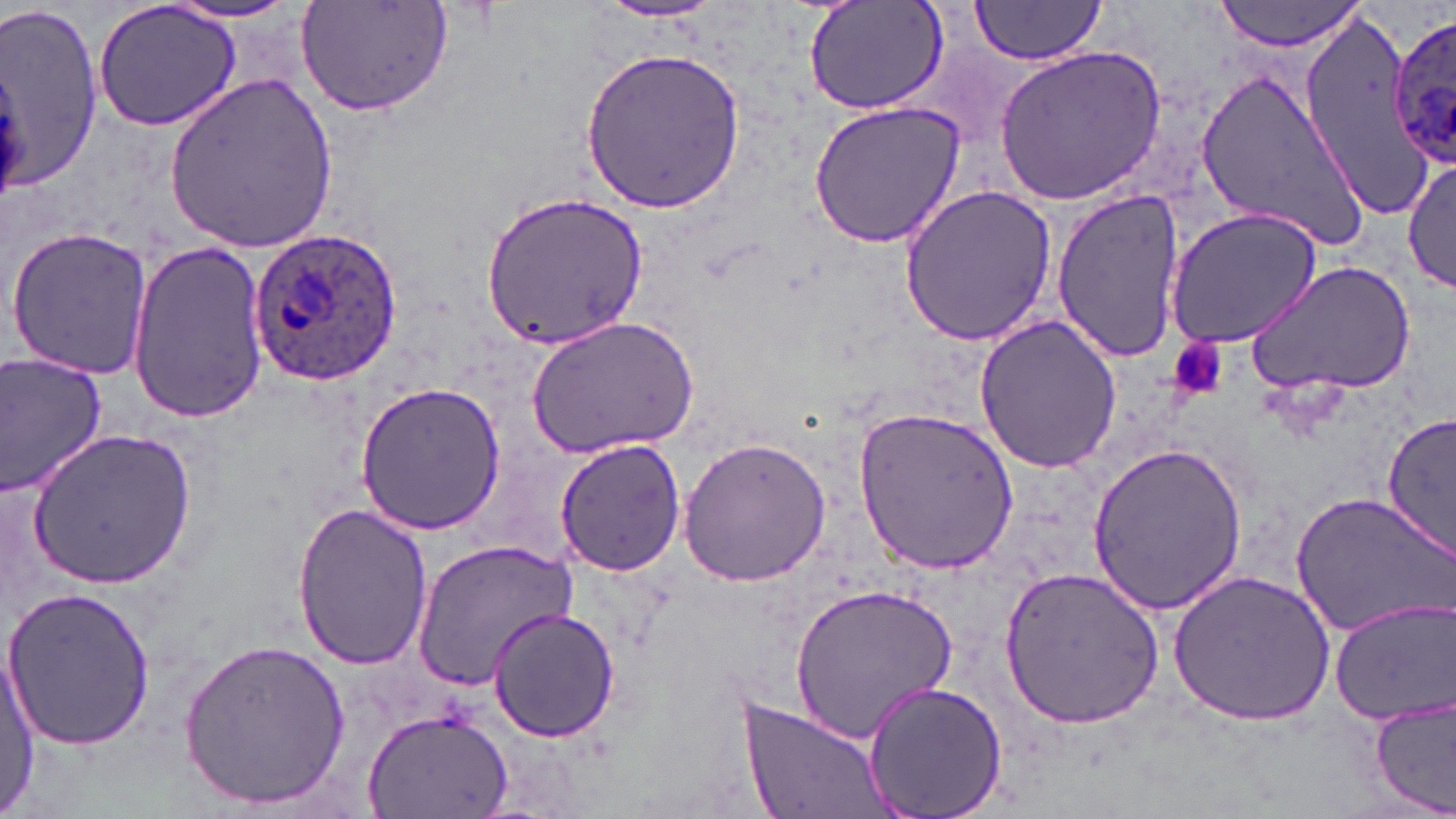

slide-level diagnosis = Plasmodium ovale
magnification = 1000x
preparation = thin blood smear
field of view = one of a larger specimen
Plasmodium ovale-infected red blood cell locations = approximate bounding boxes as [x1, y1, x2, y2] in pixels: [1387, 16, 1456, 166], [245, 231, 403, 385]
stain = May-Grünwald-Giemsa
image size = 1456×819 pixels
modality = light microscopy
uninfected red blood cell locations = approximate bounding boxes as [x1, y1, x2, y2] in pixels: [294, 0, 452, 116], [803, 0, 951, 118], [968, 0, 1108, 64], [1213, 0, 1366, 51], [92, 1, 245, 132], [159, 1, 306, 25], [596, 1, 728, 23], [0, 4, 107, 190], [1295, 6, 1433, 217], [581, 46, 747, 212], [995, 46, 1166, 203], [1194, 66, 1369, 251], [164, 76, 343, 250], [809, 101, 965, 248], [1404, 156, 1456, 294], [899, 185, 1057, 347], [481, 189, 648, 348], [1050, 189, 1191, 359], [1165, 207, 1321, 349], [4, 224, 157, 380], [123, 239, 267, 422], [1245, 260, 1414, 399], [530, 314, 701, 458], [973, 315, 1122, 474], [0, 353, 109, 497], [355, 381, 507, 534], [854, 406, 1025, 573], [1382, 410, 1456, 560], [27, 427, 195, 589], [676, 435, 833, 590], [555, 440, 686, 578], [1088, 440, 1248, 617], [1291, 491, 1455, 640], [290, 502, 434, 671], [410, 539, 580, 691], [999, 567, 1165, 730], [1168, 571, 1334, 726], [789, 582, 956, 744], [1, 585, 157, 752], [1330, 599, 1455, 723], [485, 605, 622, 742], [179, 637, 351, 810], [1, 653, 39, 816], [861, 678, 1008, 819], [732, 695, 897, 819], [1371, 695, 1456, 817], [365, 705, 515, 818]